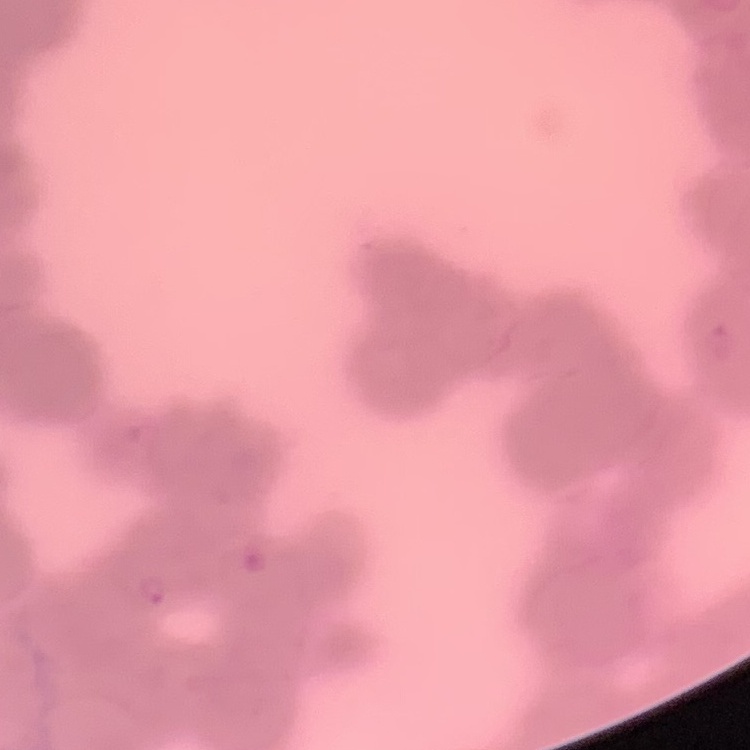
{
  "red_blood_cell_morphology": "rouleaux formation",
  "image_type": "one tile cut from a larger photomicrograph",
  "stain": "Field's or Giemsa",
  "preparation": "thin blood smear"
}